Evaluate for Plasmodium parasites.
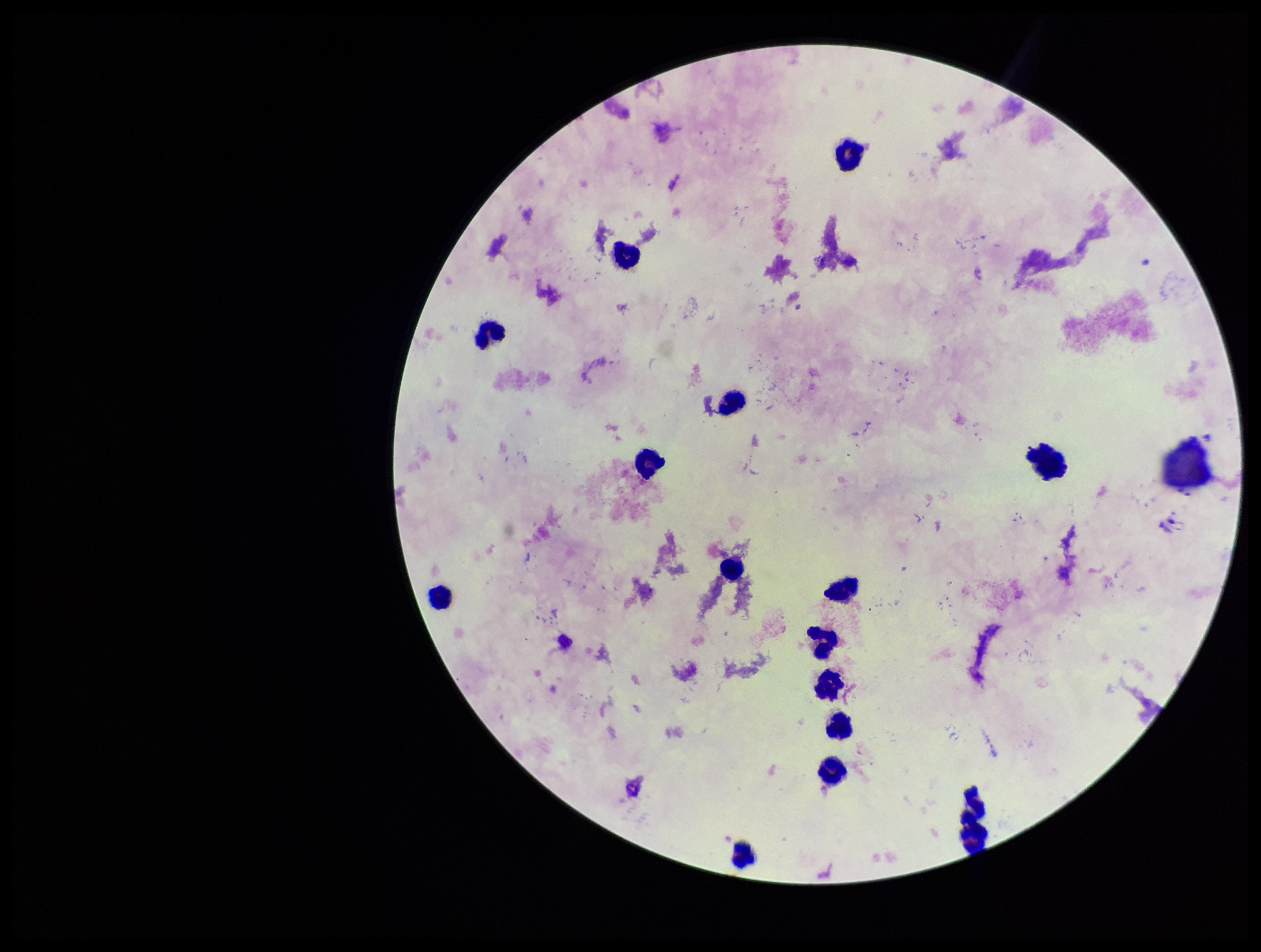

None identified.

capture = smartphone photograph through the microscope eyepiece
field of view = single
parasite count = 0
leukocyte count = 15
preparation = thick
image size = 1261×952 pixels
patient malaria status = negative
stain = Giemsa